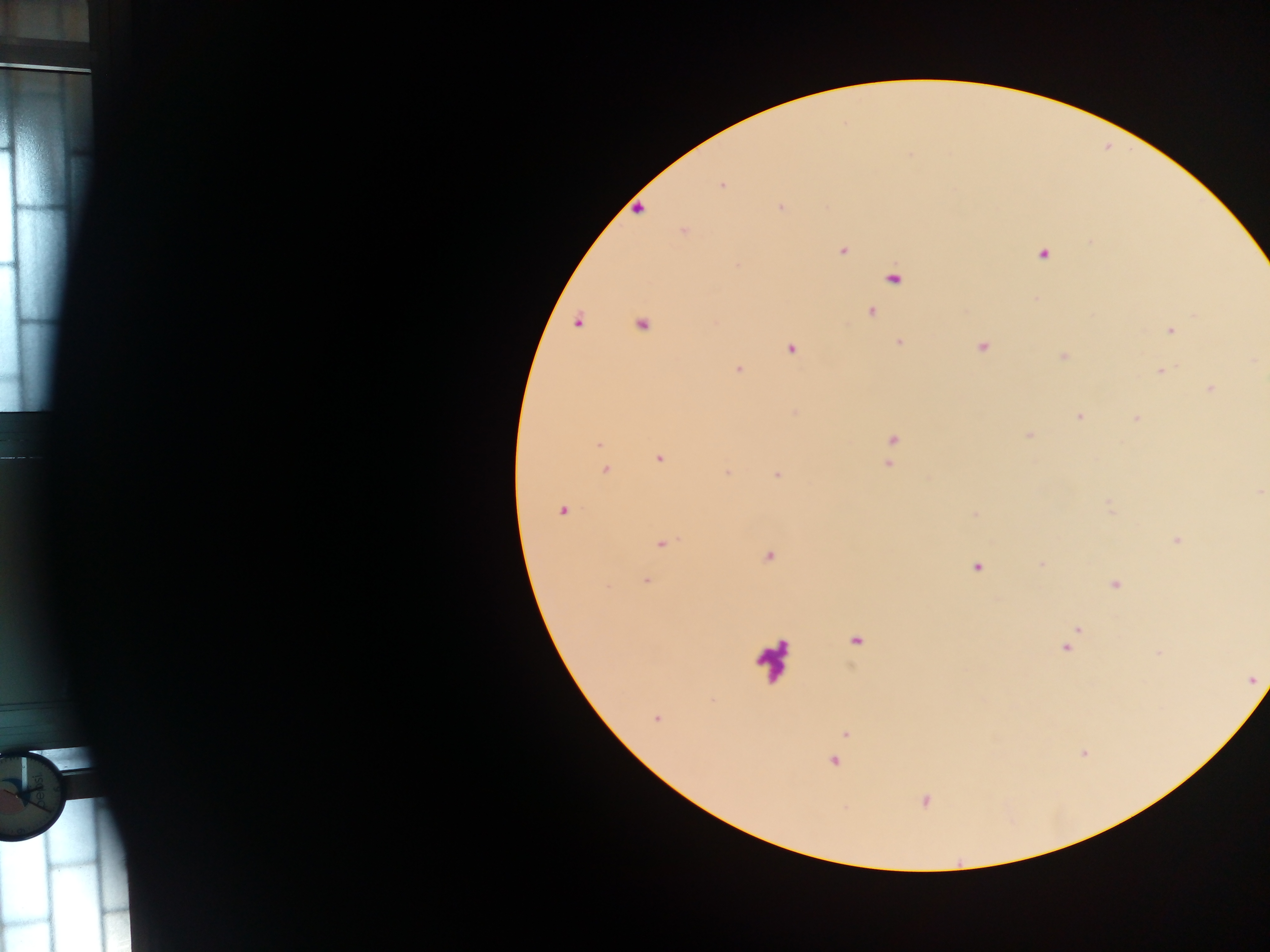
Approximate centers as {x, y} in pixels. Leukocyte locations: {772, 659}. Malaria parasite locations: {721, 185}, {638, 208}, {781, 208}, {684, 231}, {842, 250}, {1043, 254}, {892, 277}, {870, 311}, {578, 320}, {640, 323}, {1170, 329}, {899, 342}, {980, 346}, {790, 348}, {1063, 356}, {1254, 359}, {738, 369}, {1161, 370}, {1210, 388}, {795, 411}, {1080, 416}, {1137, 418}, {1028, 435}, {892, 439}, {599, 444}, {658, 458}, {887, 464}, {605, 469}, {726, 472}, {776, 474}, {1259, 491}, {1108, 504}, {562, 510}, {974, 514}, {1177, 540}, {660, 542}, {769, 556}, {1042, 564}, {977, 566}, {645, 581}, {1115, 584}, {1077, 628}, {854, 640}, {1066, 647}, {1159, 653}, {1251, 679}, {656, 718}, {845, 733}, {1083, 752}, {834, 761}, {924, 800}. One field of view. Image is 1270×952 pixels. Thick blood smear. Collected in Ghana. Mobile-phone photograph taken through the microscope.